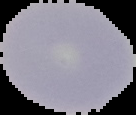

preparation = thin blood film
result = no Plasmodium parasites detected
image size = 136×115 pixels
image type = segmented cell region with the area outside set to black